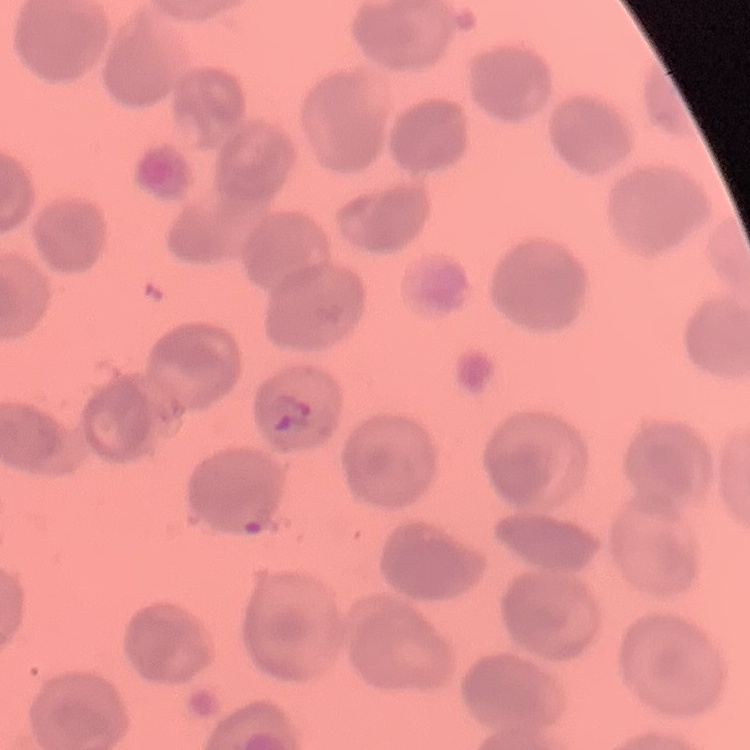
erythrocyte morphology = no rouleaux formation
preparation = thin blood smear
image type = square crop of a larger photomicrograph
stain = Field's or Giemsa